Report the malaria status of this cell.
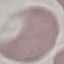
It is uninfected.

image type = automatically extracted cell patch, resized to 64 × 64 pixels
capture = smartphone through the microscope eyepiece
preparation = thin smear
stain = Giemsa